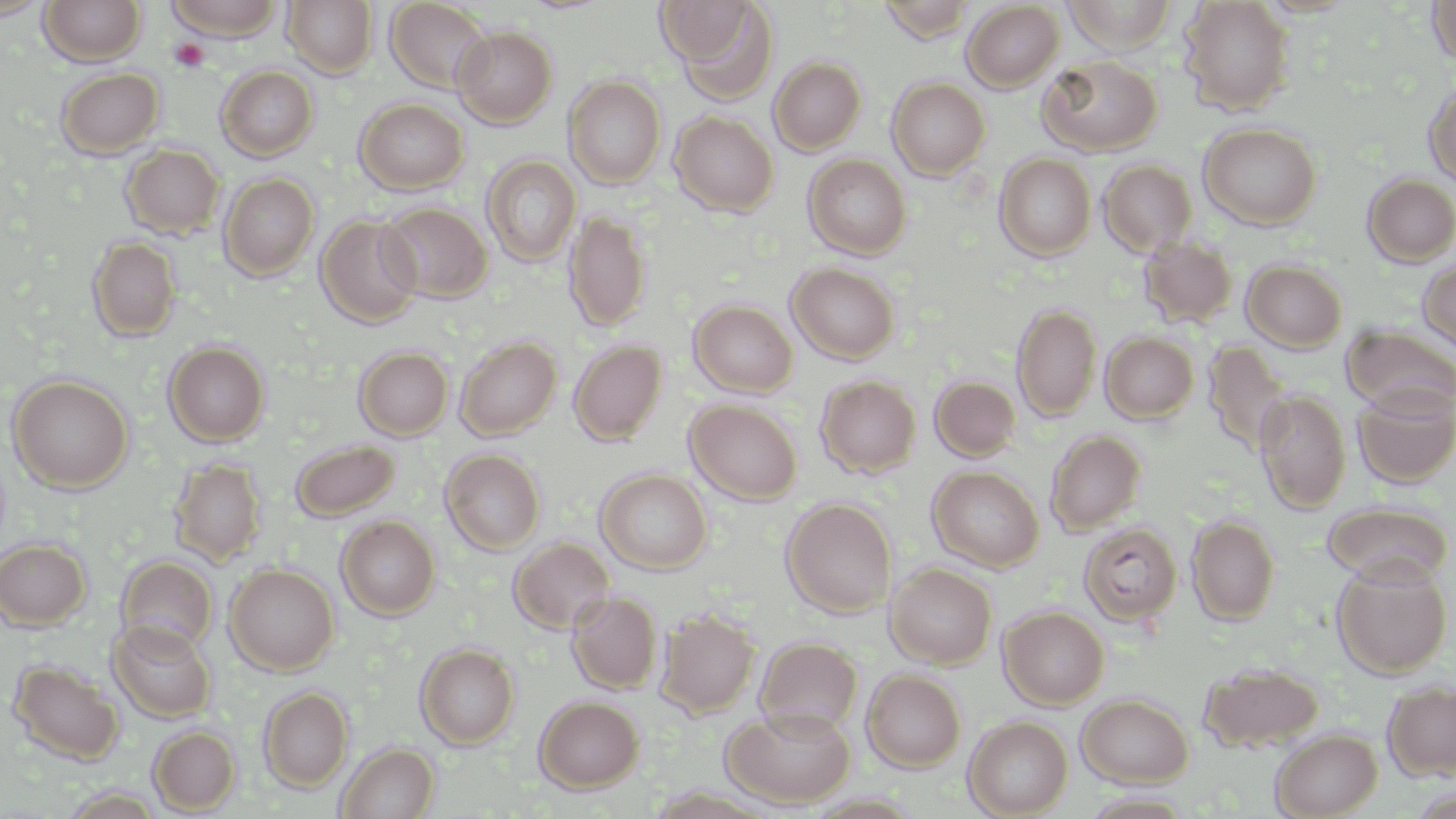
Summary:
  - Coordinate format: approximate bounding boxes as [x1, y1, x2, y2] in pixels
  - Uninfected red blood cell locations: [0, 0, 51, 19], [39, 0, 146, 66], [165, 0, 285, 41], [283, 0, 378, 78], [385, 0, 493, 93], [875, 0, 977, 42], [1062, 0, 1179, 54], [1179, 0, 1295, 115], [1427, 0, 1456, 65], [961, 1, 1065, 92], [656, 2, 755, 64], [668, 2, 780, 105], [452, 25, 558, 128], [1038, 54, 1162, 155], [769, 56, 866, 154], [216, 66, 318, 161], [56, 67, 164, 158], [564, 76, 666, 188], [887, 77, 990, 180], [1423, 81, 1456, 188], [355, 98, 469, 194], [670, 111, 779, 216], [1198, 122, 1322, 229], [121, 144, 225, 239], [994, 153, 1096, 261], [481, 154, 581, 267], [804, 154, 912, 260], [1098, 159, 1197, 256], [219, 173, 319, 280], [1361, 173, 1456, 266], [378, 202, 493, 303], [564, 209, 651, 332], [316, 214, 423, 327], [1139, 235, 1238, 327], [88, 236, 181, 342], [1417, 258, 1456, 352], [1241, 259, 1347, 351], [787, 262, 901, 363], [689, 300, 798, 397], [1011, 303, 1102, 422], [1341, 324, 1456, 415], [1100, 331, 1199, 423], [456, 336, 561, 439], [1203, 339, 1292, 455], [569, 340, 667, 445], [164, 341, 270, 447], [354, 346, 453, 440], [8, 375, 133, 492], [815, 375, 921, 477], [930, 376, 1020, 461], [1352, 384, 1456, 488], [1254, 389, 1351, 513], [685, 399, 802, 504], [1045, 430, 1146, 536], [290, 439, 400, 521], [441, 448, 546, 554], [169, 458, 266, 567], [928, 465, 1044, 571], [595, 469, 712, 574], [781, 497, 897, 618], [1323, 502, 1454, 586], [1186, 515, 1280, 625], [336, 516, 440, 620], [1078, 522, 1182, 626], [0, 538, 91, 630], [509, 538, 615, 634], [116, 555, 218, 655], [1332, 560, 1452, 678], [886, 563, 997, 669], [225, 564, 339, 674], [567, 591, 662, 694], [998, 606, 1109, 708], [656, 609, 760, 718], [108, 619, 216, 723], [755, 637, 862, 734], [415, 643, 519, 749], [8, 659, 124, 765], [1200, 662, 1324, 751], [862, 669, 966, 772], [1383, 680, 1456, 781], [258, 686, 353, 791], [1076, 693, 1194, 787], [534, 696, 644, 793], [722, 707, 856, 809], [963, 716, 1073, 818], [148, 726, 239, 813], [1270, 728, 1382, 819], [336, 742, 438, 819], [1081, 791, 1198, 818]
  - Platelet locations: [169, 39, 210, 72]
  - Slide-level diagnosis: negative for blood parasites
  - Modality: light microscopy
  - Field of view: single
  - Stain: May-Grünwald-Giemsa
  - Image size: 1456×819 pixels
  - Magnification: 1000x
  - Preparation: thin blood smear